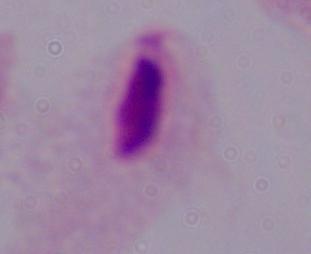
Summary:
  - Magnification: 1000x
  - Modality: photomicrograph
  - Identification: trichomonad